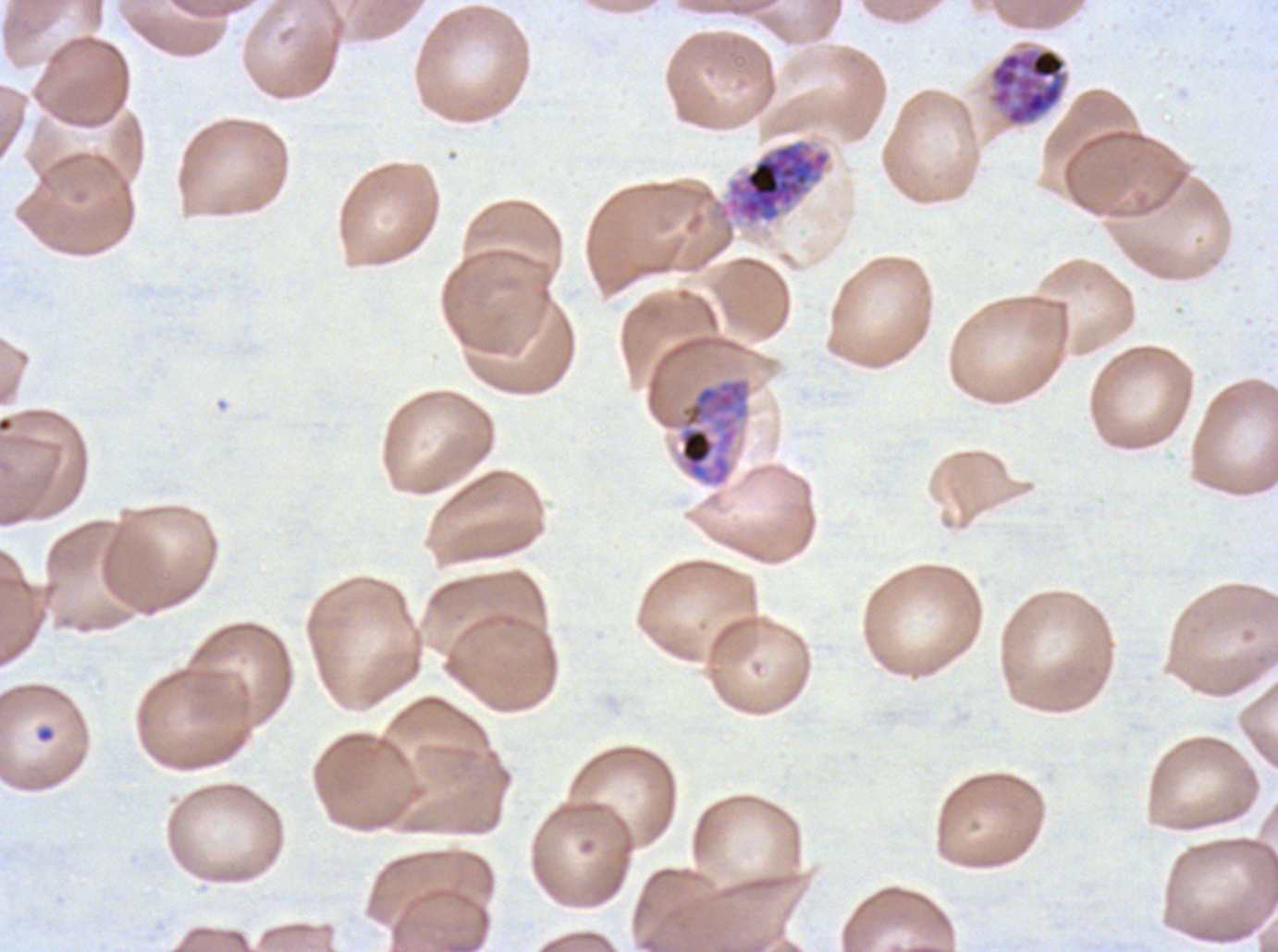
notation = approximate bounding rectangles given as corner coordinates in pixels from the top-left
ring locations = (x1=35, y1=726, x2=55, y2=743)
late schizont locations = (x1=989, y1=47, x2=1067, y2=126), (x1=717, y1=140, x2=831, y2=225), (x1=678, y1=377, x2=751, y2=487)
preparation = thin blood smear
specimen = P. falciparum from a patient in The Gambia, cultured ex vivo for 24 to 48 hours
life-cycle stages observed = ring, late schizont
stain = Giemsa
field of view = one sub-image of a larger composite
image size = 1278×952 pixels